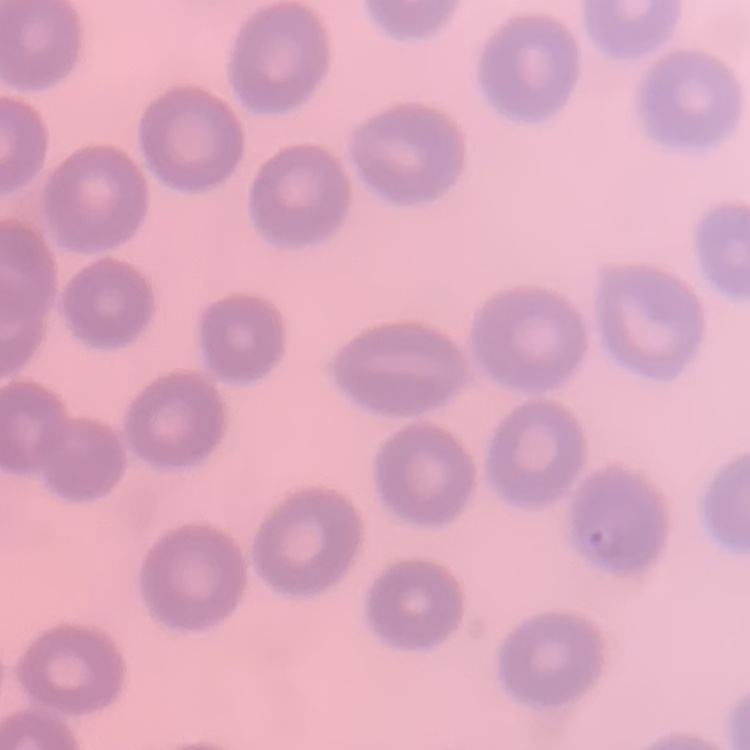
The red blood cells show no rouleaux formation. One tile cut from a larger photomicrograph. Stained with either Field's or Giemsa. Thin peripheral smear.